Locate and identify every blood parasite.
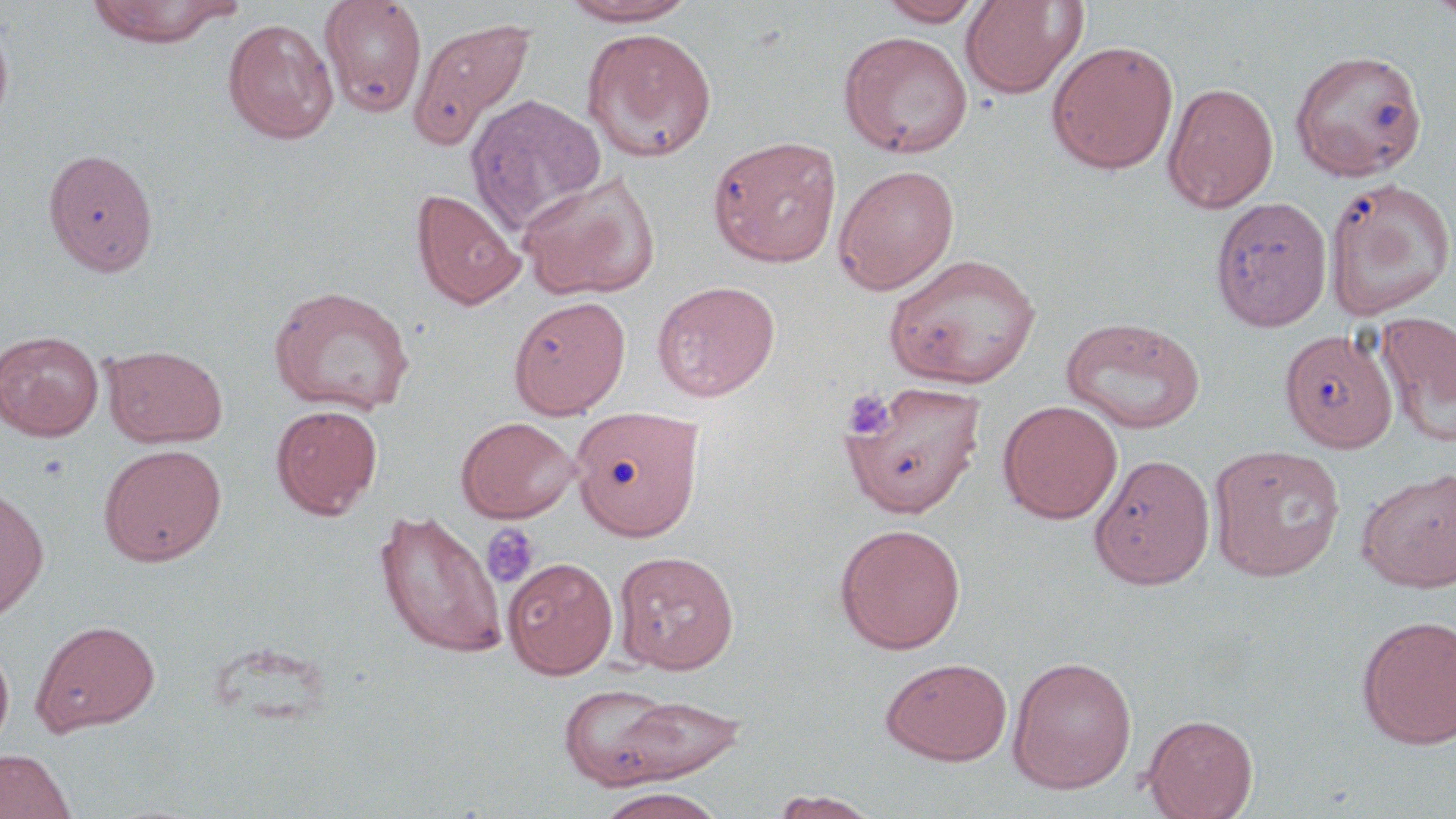

No blood parasites observed.

Summary:
  - Coordinate format: approximate bounding boxes as named x1/y1/x2/y2 corners in pixels
  - Uninfected red blood cell locations: (x1=319, y1=0, x2=428, y2=117), (x1=560, y1=0, x2=700, y2=27), (x1=878, y1=0, x2=986, y2=26), (x1=959, y1=0, x2=1088, y2=99), (x1=1425, y1=0, x2=1456, y2=25), (x1=87, y1=1, x2=237, y2=47), (x1=0, y1=16, x2=14, y2=136), (x1=409, y1=16, x2=536, y2=150), (x1=223, y1=18, x2=339, y2=144), (x1=582, y1=27, x2=717, y2=163), (x1=839, y1=30, x2=973, y2=158), (x1=1046, y1=40, x2=1180, y2=174), (x1=1290, y1=48, x2=1426, y2=182), (x1=1162, y1=81, x2=1279, y2=214), (x1=465, y1=92, x2=607, y2=236), (x1=707, y1=135, x2=843, y2=268), (x1=43, y1=148, x2=159, y2=276), (x1=833, y1=164, x2=960, y2=295), (x1=516, y1=169, x2=660, y2=301), (x1=1324, y1=177, x2=1455, y2=320), (x1=411, y1=188, x2=526, y2=310), (x1=1209, y1=196, x2=1332, y2=331), (x1=884, y1=253, x2=1041, y2=389), (x1=651, y1=280, x2=781, y2=401), (x1=268, y1=284, x2=415, y2=416), (x1=508, y1=296, x2=631, y2=419), (x1=1375, y1=310, x2=1455, y2=446), (x1=1060, y1=317, x2=1207, y2=435), (x1=1280, y1=328, x2=1398, y2=452), (x1=0, y1=330, x2=104, y2=441), (x1=102, y1=344, x2=227, y2=447), (x1=840, y1=381, x2=987, y2=517), (x1=997, y1=399, x2=1123, y2=524), (x1=271, y1=404, x2=383, y2=519), (x1=570, y1=405, x2=703, y2=540), (x1=456, y1=416, x2=580, y2=523), (x1=98, y1=444, x2=227, y2=566), (x1=1207, y1=444, x2=1346, y2=581), (x1=1089, y1=453, x2=1216, y2=590), (x1=1356, y1=466, x2=1456, y2=593), (x1=0, y1=486, x2=49, y2=623), (x1=373, y1=510, x2=508, y2=658), (x1=834, y1=522, x2=967, y2=655), (x1=613, y1=550, x2=739, y2=674), (x1=503, y1=557, x2=618, y2=679), (x1=1355, y1=614, x2=1456, y2=749), (x1=31, y1=619, x2=160, y2=736), (x1=0, y1=637, x2=15, y2=755), (x1=1007, y1=655, x2=1138, y2=794), (x1=881, y1=658, x2=1012, y2=764), (x1=560, y1=685, x2=745, y2=788), (x1=1141, y1=714, x2=1258, y2=819), (x1=0, y1=748, x2=78, y2=819), (x1=595, y1=787, x2=729, y2=819), (x1=770, y1=789, x2=880, y2=818)
  - Platelet locations: (x1=842, y1=389, x2=895, y2=440), (x1=481, y1=522, x2=541, y2=589)
  - Slide-level diagnosis: negative for blood parasites
  - Magnification: 1000x
  - Preparation: thin blood film
  - Modality: light microscopy
  - Stain: May-Grünwald-Giemsa
  - Image size: 1456×819 pixels
  - Field of view: one of a larger specimen